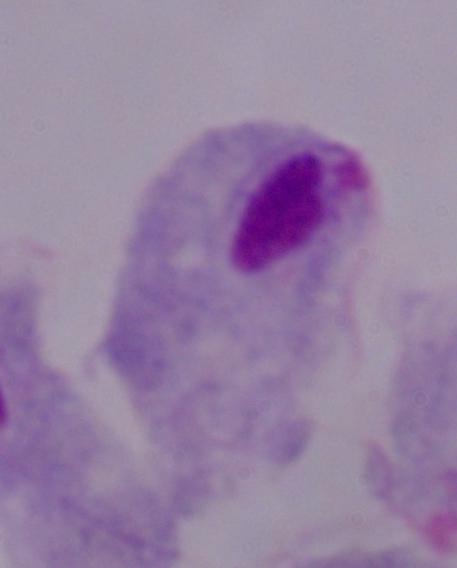
modality = micrograph
identification = trichomonad
magnification = 1000x